Outline each Plasmodium falciparum-infected red blood cell.
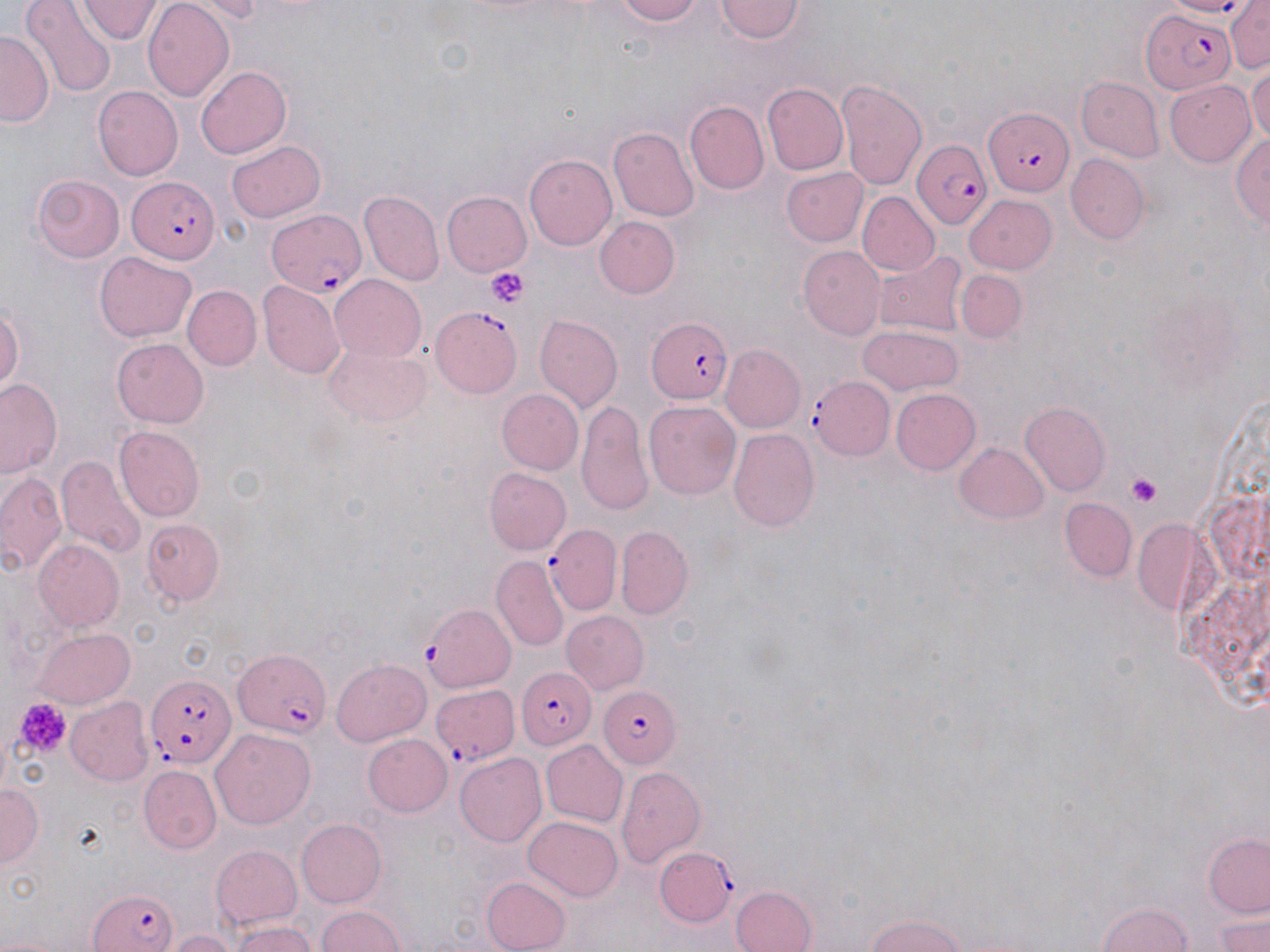

Approximate bounding boxes as (x1, y1, x2, y2) in pixels.
Plasmodium falciparum-infected red blood cells (subset): (1138, 9, 1237, 95), (984, 107, 1073, 192), (911, 138, 994, 230), (128, 176, 221, 263), (265, 209, 367, 296), (429, 303, 524, 397), (643, 316, 734, 405), (810, 377, 895, 459), (547, 525, 620, 611), (422, 602, 516, 690), (231, 650, 331, 734), (517, 668, 597, 748), (147, 670, 238, 769), (600, 687, 683, 767), (655, 848, 736, 928), (86, 885, 180, 952).

Platelet locations: (487, 268, 529, 308), (1126, 472, 1161, 509), (14, 698, 69, 756). Uninfected red blood cell locations (subset): (24, 0, 114, 96), (608, 0, 711, 25), (714, 0, 806, 43), (1228, 1, 1270, 74), (77, 2, 160, 46), (144, 3, 235, 102), (0, 28, 51, 127), (196, 63, 292, 158), (1249, 66, 1270, 150), (836, 77, 929, 194), (1074, 77, 1163, 161), (1163, 78, 1257, 165), (763, 83, 847, 173), (93, 87, 182, 178), (686, 100, 769, 193), (612, 127, 700, 222), (1232, 130, 1270, 234), (228, 137, 326, 222), (525, 152, 616, 248), (1066, 153, 1150, 243), (782, 168, 867, 247), (32, 174, 126, 263), (359, 190, 444, 285), (440, 191, 531, 278), (857, 192, 939, 277), (964, 192, 1057, 272), (595, 216, 680, 298), (800, 247, 886, 339), (873, 250, 969, 336), (95, 252, 196, 342), (956, 270, 1027, 343), (328, 273, 427, 362), (258, 279, 346, 377), (184, 286, 261, 370), (0, 296, 23, 399), (535, 314, 623, 413), (856, 328, 964, 395), (112, 338, 211, 427), (324, 341, 431, 428), (722, 344, 807, 433), (0, 379, 63, 480), (890, 389, 980, 474), (498, 390, 583, 474), (577, 399, 654, 516), (644, 401, 741, 500), (1021, 403, 1111, 497), (113, 425, 204, 522), (729, 427, 820, 531), (954, 441, 1051, 524), (57, 456, 144, 558), (485, 466, 572, 554), (0, 470, 67, 577), (1061, 499, 1139, 580), (143, 515, 227, 606), (616, 524, 693, 616), (33, 539, 124, 631), (490, 556, 568, 650), (562, 611, 648, 694), (31, 624, 136, 709), (330, 655, 431, 745), (68, 698, 154, 785), (210, 725, 314, 825), (361, 733, 453, 817), (542, 739, 628, 826), (455, 752, 547, 846), (617, 764, 706, 867), (141, 767, 221, 852), (1, 781, 42, 869), (523, 816, 624, 900), (295, 818, 387, 908), (1202, 834, 1270, 919), (211, 843, 303, 930), (480, 875, 571, 952), (731, 887, 815, 952), (1095, 902, 1199, 952), (313, 904, 407, 952), (1212, 910, 1270, 951), (860, 913, 976, 952), (231, 922, 318, 952), (165, 929, 241, 952). Slide-level diagnosis: Plasmodium falciparum. Image is 1270×952 pixels. Optical microscopy. May-Grünwald-Giemsa-stained preparation. One field of a larger specimen. Thin blood film. 1000x magnification.